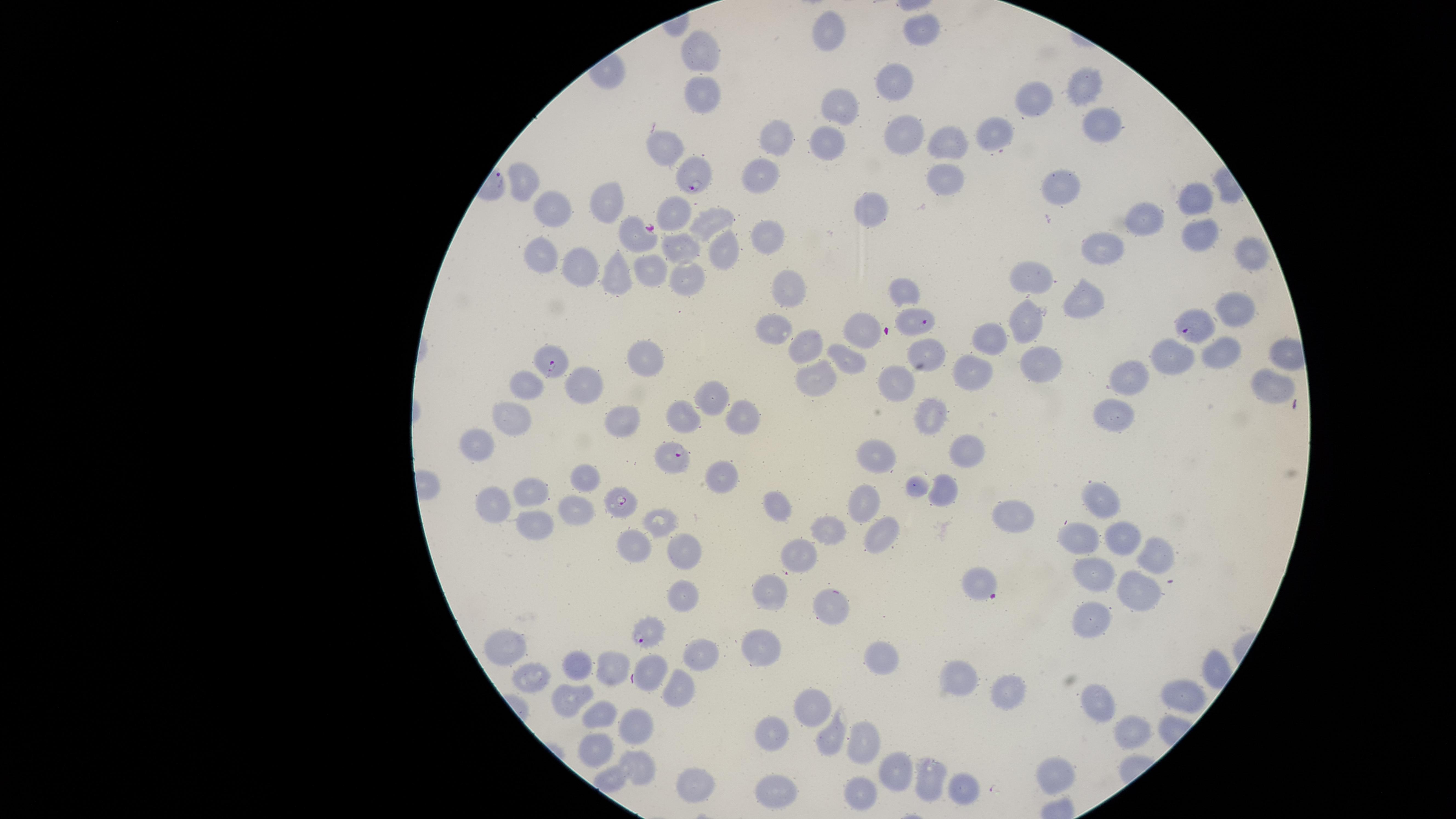

Approximate marker points as {x, y} in pixels.
Summary:
  - Uninfected RBCs: {917, 29}, {830, 32}, {705, 53}, {892, 78}, {1085, 88}, {703, 99}, {1033, 99}, {840, 109}, {1106, 125}, {994, 132}, {776, 136}, {908, 136}, {664, 140}, {954, 140}, {829, 145}, {758, 175}, {947, 175}, {530, 180}, {1069, 180}, {1189, 196}, {607, 203}, {867, 203}, {558, 211}, {681, 213}, {1148, 217}, {710, 222}, {1197, 229}, {767, 234}, {1109, 244}, {684, 247}, {729, 249}, {1249, 255}, {545, 261}, {575, 268}, {652, 269}, {619, 273}, {682, 280}, {1039, 280}, {788, 288}, {904, 288}, {1084, 295}, {1238, 307}, {1029, 323}, {768, 328}, {996, 332}, {864, 333}, {810, 345}, {926, 353}, {642, 354}, {1177, 354}, {1220, 354}, {1039, 358}, {849, 363}, {982, 369}, {1127, 370}, {588, 380}, {888, 384}, {817, 385}, {1268, 385}, {526, 386}, {714, 395}, {932, 410}, {747, 411}, {683, 414}, {1106, 414}, {509, 418}, {627, 423}, {485, 438}, {968, 451}, {883, 459}, {722, 478}, {586, 479}, {532, 488}, {947, 489}, {498, 500}, {1102, 500}, {868, 501}, {577, 509}, {776, 509}, {1004, 520}, {534, 524}, {659, 524}, {831, 534}, {1079, 537}, {1122, 540}, {883, 543}, {631, 547}, {689, 553}, {804, 555}, {1154, 555}, {976, 578}, {1099, 578}, {1139, 590}, {778, 591}, {685, 597}, {832, 603}, {1093, 617}, {767, 644}, {507, 650}, {700, 650}, {884, 656}, {614, 671}, {580, 672}, {648, 672}, {963, 679}, {528, 681}, {1006, 691}, {682, 693}, {1179, 693}, {567, 701}, {1101, 703}, {815, 706}, {598, 717}, {637, 723}, {777, 725}, {1133, 729}, {865, 736}, {830, 737}, {599, 739}, {642, 765}, {896, 773}, {929, 774}, {1053, 776}, {684, 785}, {769, 785}, {965, 786}, {856, 793}
  - Parasitized RBCs: {696, 177}, {637, 235}, {914, 322}, {1197, 329}, {548, 364}, {671, 460}, {620, 501}, {649, 632}
  - Presence: malaria parasites seen
  - Species: Plasmodium falciparum
  - Capture: smartphone photograph through the microscope eyepiece
  - Image size: 1456×819 pixels
  - Stain: Giemsa
  - Visible region: circular
  - Preparation: thin blood smear
  - Field of view: single